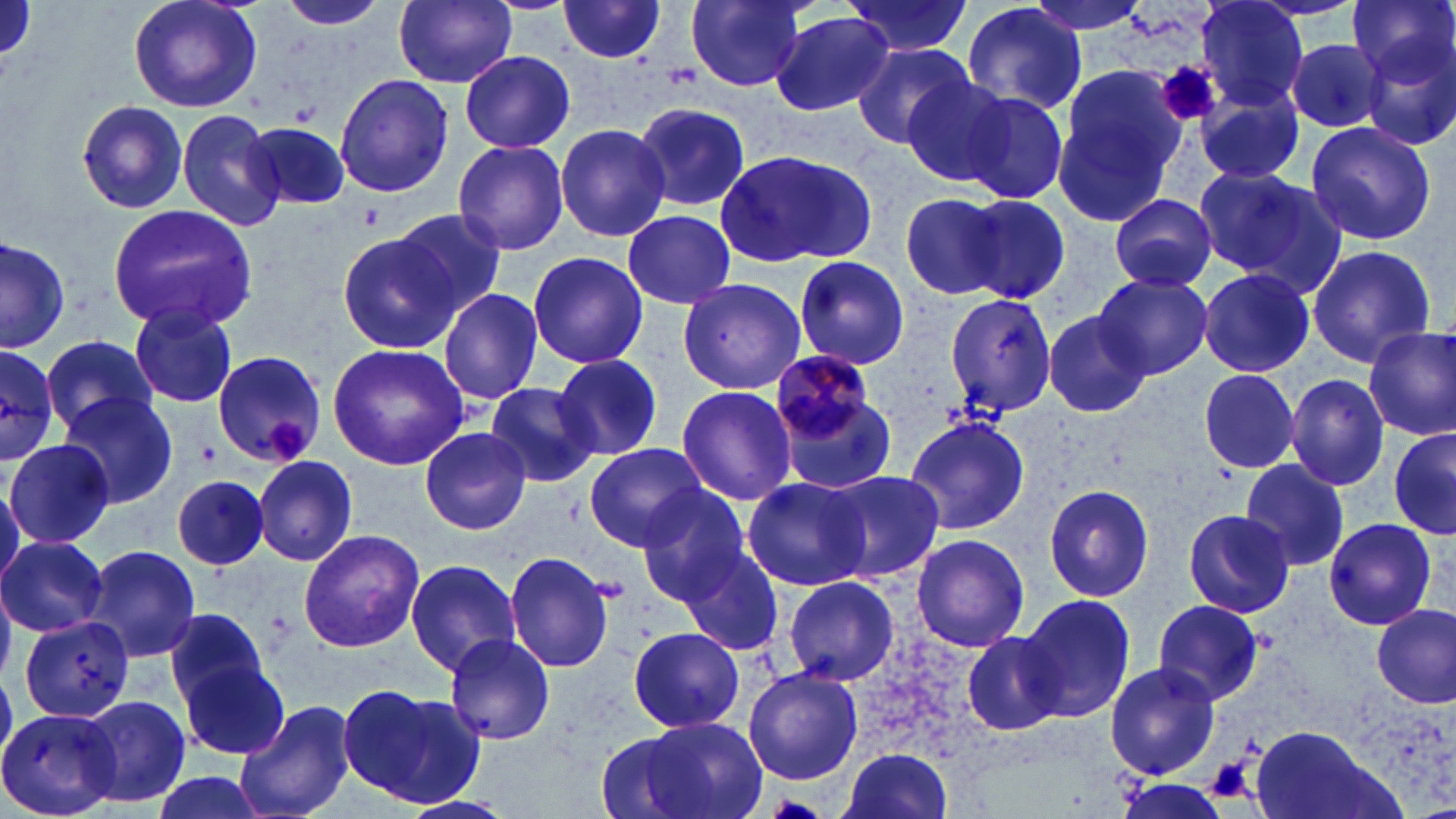
Summary:
  - Coordinate format: approximate bounding boxes as (x1,y1)-(x2,y2) corner pairs in pixels
  - Platelet locations: (1161,60)-(1221,126), (263,418)-(308,463), (198,441)-(221,467), (1205,758)-(1254,801)
  - Uninfected red blood cell locations: (125,0)-(263,114), (274,0)-(390,30), (687,0)-(809,91), (840,0)-(975,57), (1019,0)-(1151,36), (1349,0)-(1454,86), (394,1)-(518,88), (556,1)-(669,63), (960,3)-(1089,116), (1196,3)-(1310,109), (768,10)-(895,118), (1362,30)-(1456,154), (1284,37)-(1386,134), (850,40)-(974,150), (460,50)-(574,153), (1052,67)-(1188,227), (334,73)-(453,198), (898,73)-(1021,184), (943,83)-(1072,204), (1196,90)-(1306,188), (76,100)-(187,214), (630,102)-(754,211), (177,108)-(286,232), (1304,120)-(1437,245), (244,121)-(353,210), (554,122)-(669,243), (451,139)-(570,256), (713,148)-(881,268), (1190,165)-(1339,286), (902,190)-(1013,299), (1110,192)-(1217,293), (965,195)-(1070,305), (109,205)-(258,332), (392,208)-(507,317), (622,208)-(736,308), (335,231)-(458,353), (0,233)-(70,354), (0,236)-(72,354), (1307,242)-(1437,369), (527,251)-(649,370), (792,258)-(913,369), (1200,269)-(1314,377), (1093,272)-(1211,379), (677,277)-(807,393), (439,287)-(544,402), (939,291)-(1061,418), (129,304)-(238,409), (1042,311)-(1150,419), (1363,326)-(1455,442), (41,334)-(159,437), (326,342)-(471,471), (0,343)-(61,460), (212,351)-(327,465), (211,352)-(328,468), (553,354)-(663,460), (1198,368)-(1301,473), (771,373)-(897,498), (1285,374)-(1390,491), (485,382)-(598,487), (675,385)-(798,505), (59,393)-(179,510), (904,415)-(1031,536), (420,425)-(533,533), (1389,427)-(1456,540), (6,438)-(114,549), (583,442)-(709,553), (254,455)-(358,566), (1240,460)-(1348,570), (823,469)-(945,583), (741,475)-(873,592), (172,476)-(272,570), (169,477)-(271,569), (1042,482)-(1156,603), (638,489)-(754,605), (1182,508)-(1296,620), (1323,517)-(1437,631), (297,529)-(428,651), (910,533)-(1030,652), (1,534)-(108,635), (84,544)-(203,663), (678,546)-(785,655), (504,551)-(615,674), (406,557)-(521,676), (782,574)-(901,687), (758,579)-(882,774), (1018,592)-(1135,723), (1153,598)-(1265,705), (1373,604)-(1454,708), (164,608)-(271,712), (22,616)-(134,723), (627,626)-(745,735), (962,631)-(1064,736), (443,632)-(556,745), (180,656)-(291,761), (1104,662)-(1221,780), (743,667)-(863,785), (337,684)-(485,809), (79,695)-(190,808), (235,699)-(359,819), (1,705)-(121,817), (629,716)-(769,819), (1250,727)-(1385,819), (591,730)-(711,819), (837,749)-(957,819), (143,770)-(271,819), (1114,780)-(1230,819)
  - Plasmodium malariae-infected red blood cell locations: (772,351)-(877,450)
  - Slide-level diagnosis: Plasmodium malariae
  - Field of view: one of a larger specimen
  - Preparation: thin blood smear
  - Modality: optical microscopy
  - Image size: 1456×819 pixels
  - Magnification: 1000x
  - Stain: May-Grünwald-Giemsa